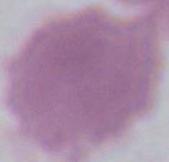
Micrograph. 1000x magnification. An erythrocyte is shown.